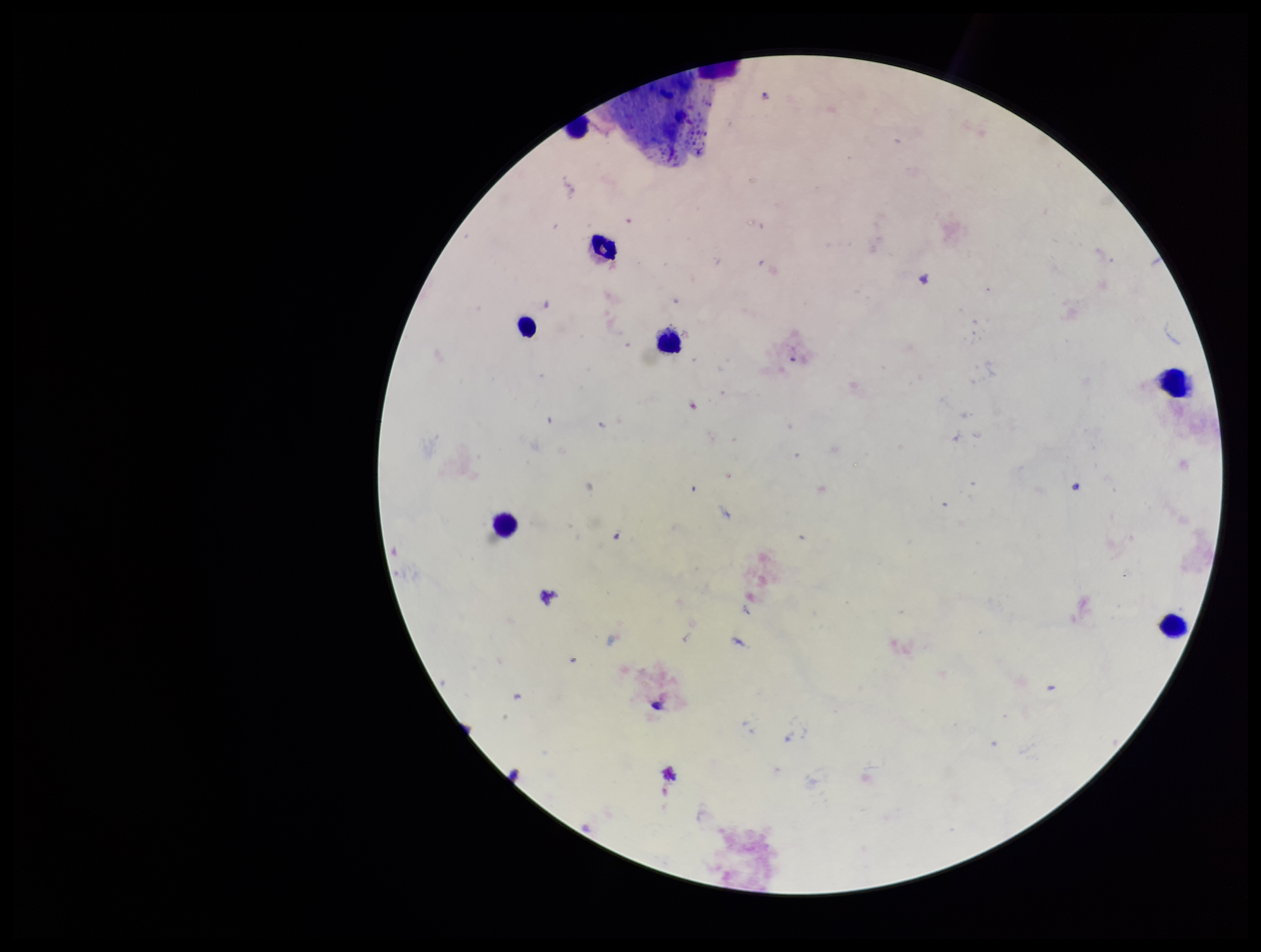

Plasmodium parasites = none seen
preparation = thick
patient malaria status = negative
capture = smartphone photograph through the microscope eyepiece
stain = Giemsa
field of view = single
image size = 1261×952 pixels
parasite count = 0
leukocyte count = 7